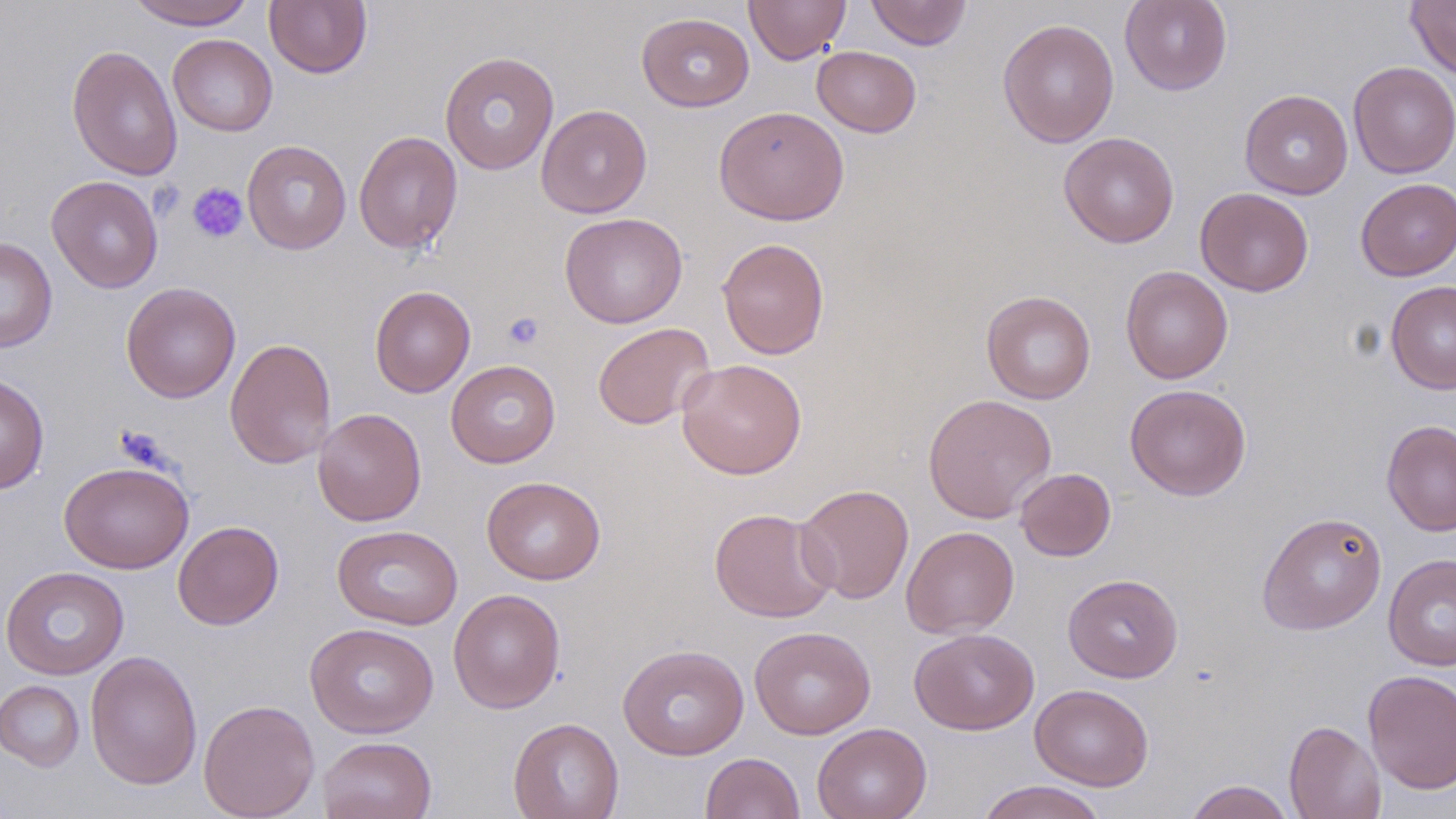 Approximate bounding boxes as [x1, y1, x2, y2] in pixels. Uninfected red blood cell locations: [127, 0, 255, 29], [264, 0, 372, 78], [744, 0, 851, 64], [865, 0, 973, 50], [1119, 0, 1232, 95], [1405, 0, 1456, 80], [636, 12, 755, 112], [997, 18, 1120, 148], [168, 34, 277, 136], [66, 44, 183, 181], [811, 45, 921, 137], [439, 50, 560, 175], [1348, 61, 1456, 179], [1239, 89, 1353, 199], [536, 104, 652, 218], [713, 105, 849, 226], [353, 130, 463, 254], [1059, 132, 1180, 248], [242, 140, 351, 254], [46, 175, 163, 293], [1356, 178, 1456, 281], [1195, 187, 1313, 297], [559, 211, 688, 329], [0, 237, 58, 353], [716, 237, 830, 360], [1120, 266, 1233, 384], [1386, 279, 1456, 394], [121, 282, 241, 403], [369, 285, 476, 398], [981, 290, 1096, 404], [593, 322, 715, 430], [224, 337, 337, 469], [676, 358, 808, 479], [446, 360, 560, 468], [0, 373, 49, 494], [1125, 383, 1251, 501], [923, 393, 1057, 523], [312, 408, 426, 526], [1381, 419, 1456, 537], [59, 461, 194, 573], [1015, 468, 1116, 561], [482, 476, 605, 584], [794, 483, 914, 604], [709, 507, 837, 623], [1257, 511, 1387, 635], [173, 520, 284, 630], [332, 524, 463, 631], [901, 525, 1019, 639], [1383, 553, 1456, 671], [1, 566, 129, 679], [1063, 574, 1183, 683], [448, 588, 565, 714], [305, 622, 439, 738], [749, 626, 876, 739], [909, 627, 1040, 735], [617, 643, 749, 760], [85, 651, 203, 791], [1362, 669, 1456, 795], [0, 679, 84, 771], [1030, 684, 1154, 790], [198, 699, 320, 819], [508, 717, 624, 819], [1284, 720, 1386, 819], [812, 723, 932, 819], [317, 735, 437, 819], [700, 752, 804, 818], [975, 780, 1109, 819], [1184, 780, 1295, 819]. Platelet locations: [187, 182, 249, 243], [503, 312, 545, 350]. Slide-level diagnosis: no evidence of blood parasites. May-Grünwald-Giemsa stain. Image is 1456×819 pixels. Optical microscopy. Thin blood film. Single field of view. 1000x magnification.